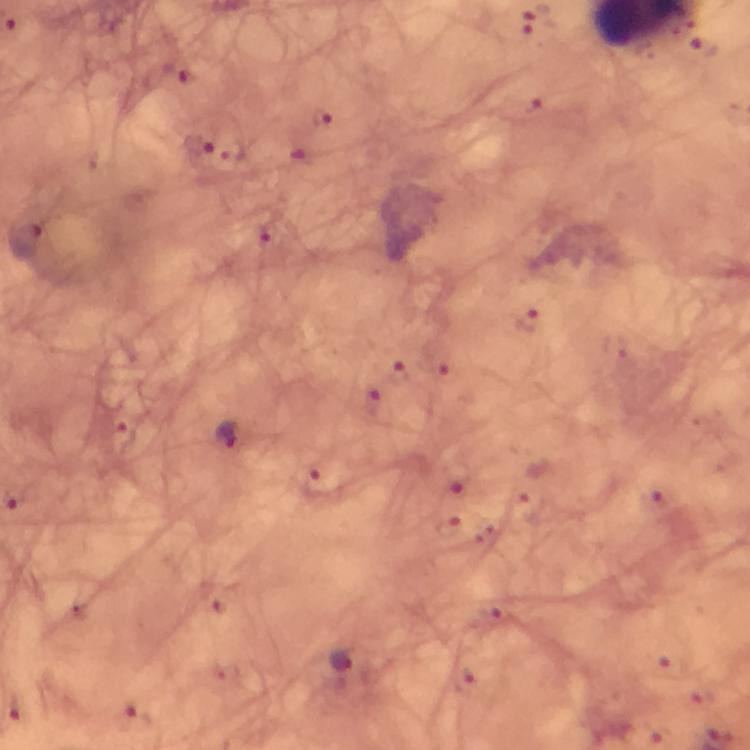

{
  "stain": "Giemsa",
  "plasmodium_parasite_locations": "approximate centers as (x, y) in pixels: (201, 149), (27, 241), (229, 436), (343, 663)",
  "preparation": "thick blood smear",
  "context": "from a diagnostic examination for malaria",
  "image_size": "750×750 pixels",
  "cropped_from": "one field of view",
  "magnification": "100x",
  "immersion_oil": "applied",
  "capture": "smartphone mounted on the microscope"
}